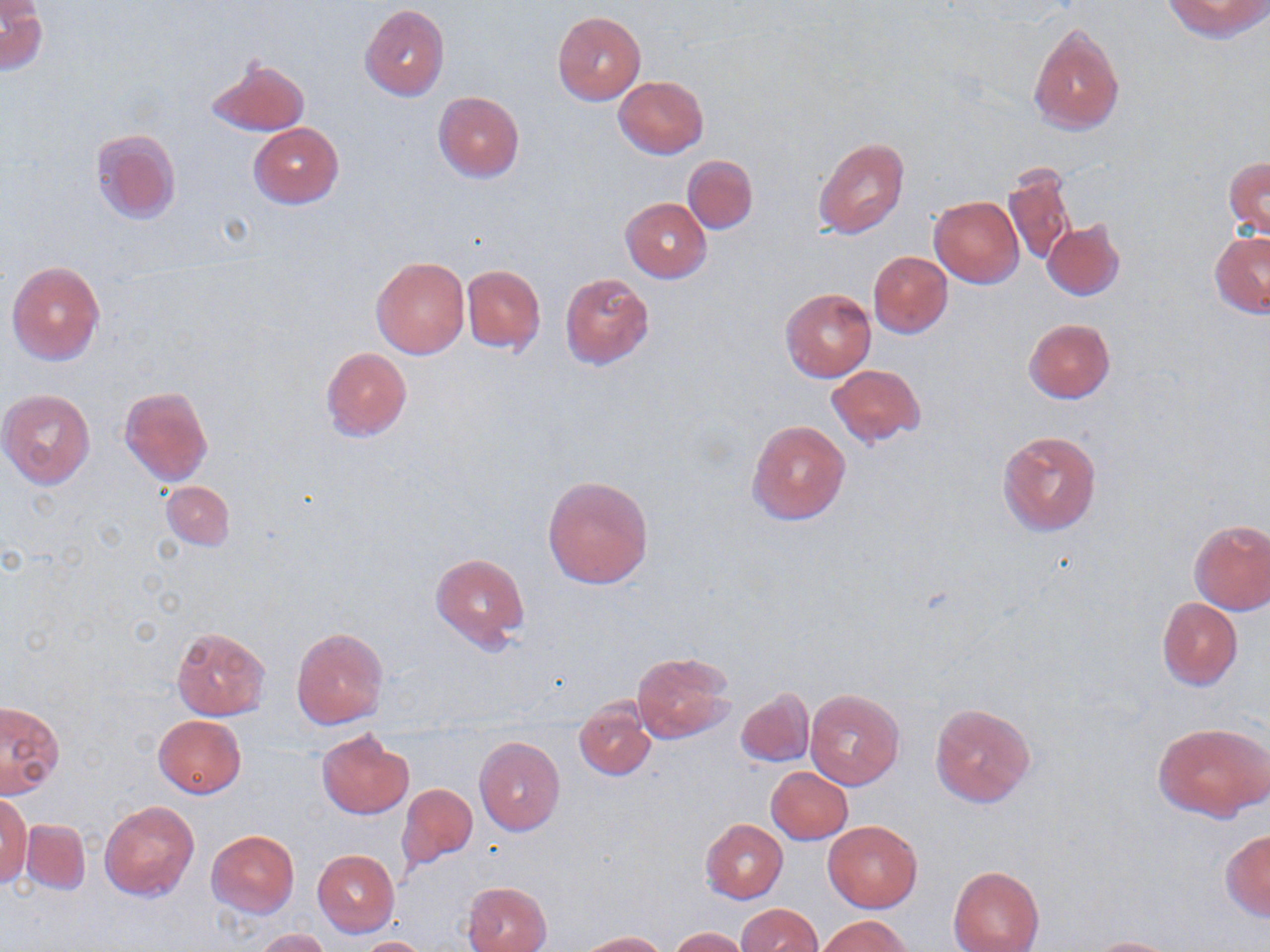

slide-level diagnosis = no evidence of blood parasites
field of view = single
uninfected red blood cell locations = approximate bounding boxes as [x1, y1, x2, y2] in pixels: [1163, 0, 1267, 42], [2, 1, 43, 27], [360, 3, 450, 100], [0, 7, 48, 76], [551, 12, 646, 104], [1026, 23, 1125, 136], [208, 58, 310, 137], [614, 76, 707, 158], [434, 92, 525, 182], [248, 122, 344, 209], [89, 128, 181, 224], [814, 138, 909, 239], [683, 155, 757, 234], [1226, 157, 1269, 236], [1003, 166, 1076, 267], [930, 197, 1023, 287], [621, 198, 712, 283], [1043, 221, 1124, 300], [1210, 232, 1270, 318], [868, 251, 952, 337], [370, 256, 470, 358], [6, 261, 104, 365], [462, 264, 545, 354], [559, 273, 654, 368], [781, 289, 875, 381], [1024, 318, 1115, 403], [321, 347, 412, 441], [826, 365, 928, 448], [119, 386, 214, 486], [1, 390, 98, 489], [747, 420, 850, 524], [997, 429, 1102, 538], [542, 473, 655, 590], [160, 480, 235, 550], [1188, 520, 1270, 614], [430, 553, 532, 650], [1157, 597, 1243, 689], [291, 626, 389, 730], [171, 628, 269, 721], [631, 653, 733, 741], [735, 688, 814, 768], [804, 688, 904, 791], [0, 700, 64, 798], [929, 702, 1036, 808], [575, 704, 656, 781], [154, 715, 245, 798], [1154, 721, 1268, 820], [318, 730, 412, 819], [474, 737, 565, 835], [767, 766, 853, 844], [398, 783, 477, 872], [1, 796, 32, 888], [101, 801, 199, 901], [21, 818, 91, 895], [701, 820, 787, 902], [823, 820, 922, 912], [207, 830, 298, 916], [1220, 830, 1270, 921], [313, 850, 399, 935], [949, 864, 1045, 952], [462, 881, 553, 952], [735, 903, 822, 952], [817, 916, 910, 952], [668, 927, 749, 952], [254, 928, 329, 952], [579, 931, 667, 951], [1083, 936, 1186, 952], [354, 937, 434, 952]
stain = May-Grünwald-Giemsa
magnification = 1000x
preparation = thin blood film
modality = light microscopy
image size = 1270×952 pixels